Locate every blood parasite and identify its species.
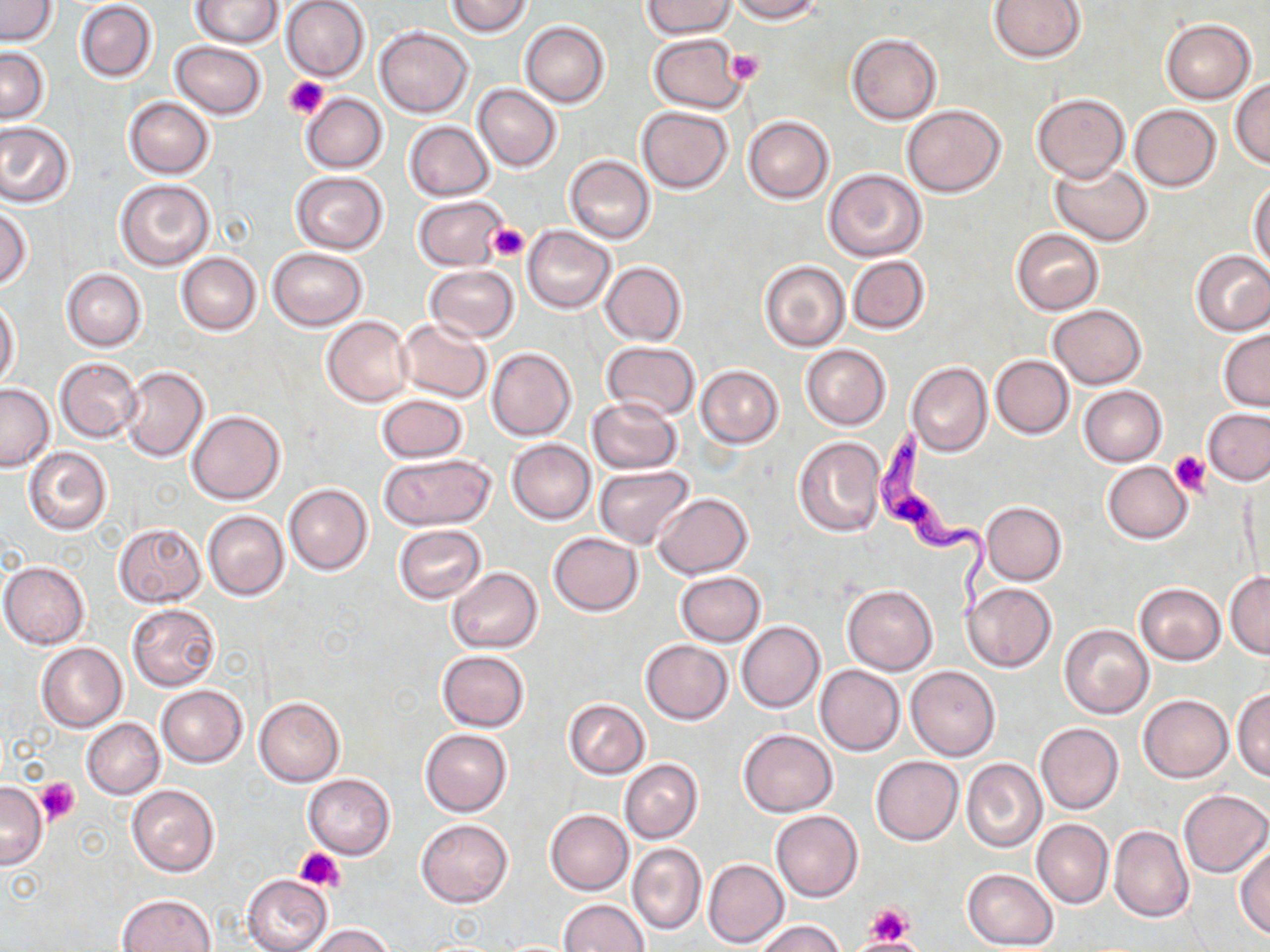

Approximate bounding boxes as (x1,y1)-(x2,y2) corner pairs in pixels.
Trypanosoma brucei: (869,428)-(993,621).
No Plasmodium falciparum, Plasmodium ovale, Plasmodium malariae, Plasmodium vivax, or Babesia divergens observed.

Uninfected red blood cell locations: (192,0)-(283,48), (447,0)-(534,37), (725,0)-(824,23), (0,1)-(59,46), (280,1)-(370,81), (641,1)-(736,37), (988,1)-(1085,63), (74,2)-(158,82), (1162,19)-(1256,103), (519,21)-(610,107), (374,26)-(473,117), (846,33)-(942,123), (648,34)-(747,114), (171,41)-(267,120), (0,47)-(50,125), (1230,78)-(1270,167), (473,84)-(561,172), (301,92)-(387,173), (1032,93)-(1129,183), (122,96)-(215,178), (1129,105)-(1221,191), (636,106)-(734,193), (902,106)-(1005,197), (743,115)-(834,203), (0,120)-(75,208), (404,121)-(495,201), (564,154)-(655,244), (1050,159)-(1153,246), (824,169)-(928,262), (290,172)-(389,254), (116,179)-(215,271), (1249,181)-(1270,272), (414,196)-(506,272), (0,205)-(32,289), (523,226)-(615,313), (1011,229)-(1104,315), (267,247)-(367,329), (1191,249)-(1270,335), (176,252)-(261,335), (847,255)-(930,334), (759,260)-(850,352), (600,262)-(686,345), (426,265)-(519,342), (60,268)-(148,350), (1,298)-(20,390), (1048,304)-(1146,388), (323,316)-(413,406), (396,319)-(492,403), (1220,329)-(1270,411), (600,341)-(700,420), (801,344)-(891,430), (486,347)-(576,441), (991,354)-(1074,439), (55,357)-(142,441), (906,362)-(991,456), (696,365)-(783,448), (120,366)-(209,462), (0,383)-(54,471), (1079,385)-(1166,466), (376,393)-(469,462), (588,398)-(681,473), (1204,408)-(1270,485), (186,410)-(285,504), (793,436)-(884,538), (506,439)-(596,524), (24,447)-(111,534), (377,453)-(496,531), (1102,461)-(1193,543), (594,465)-(694,548), (284,483)-(372,574), (654,493)-(752,578), (981,501)-(1067,585), (202,510)-(290,600), (113,523)-(206,607), (393,525)-(487,603), (548,533)-(644,615), (2,561)-(89,648), (448,566)-(542,653), (674,571)-(765,646), (1225,572)-(1270,658), (1135,583)-(1225,664), (964,584)-(1057,672), (842,585)-(937,675), (127,604)-(220,691), (736,621)-(824,711), (1059,624)-(1153,719), (640,639)-(732,724), (37,643)-(127,732), (436,650)-(531,731), (816,665)-(905,755), (906,666)-(1000,760), (156,685)-(247,767), (1232,686)-(1270,782), (1138,693)-(1232,782), (253,697)-(343,786), (564,699)-(650,779), (82,718)-(163,799), (1035,722)-(1124,814), (738,728)-(837,817), (419,729)-(512,816), (871,756)-(963,845), (962,758)-(1046,852), (619,759)-(703,843), (303,774)-(395,858), (0,781)-(47,869), (126,784)-(220,876), (1178,789)-(1270,878), (547,810)-(633,896), (771,810)-(863,901), (416,818)-(513,908), (1031,819)-(1113,907), (1110,826)-(1193,923), (627,843)-(705,936), (1235,843)-(1270,942), (703,859)-(789,948), (962,869)-(1059,950), (242,873)-(333,952), (116,893)-(218,952), (558,899)-(650,952), (755,919)-(847,952), (307,923)-(395,952). Platelet locations: (723,48)-(765,86), (284,75)-(328,119), (488,224)-(530,263), (1171,452)-(1209,496), (34,777)-(80,823), (295,846)-(346,892), (864,900)-(915,944), (851,937)-(920,951). Slide-level diagnosis: Trypanosoma brucei. Thin blood smear. Optical microscopy. Captured at 1000x magnification. Image is 1270×952 pixels. Single field of view. May-Grünwald-Giemsa-stained preparation.